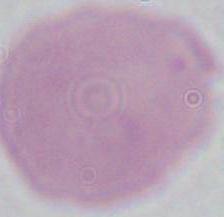
An erythrocyte is seen. Photomicrograph. 1000x magnification.